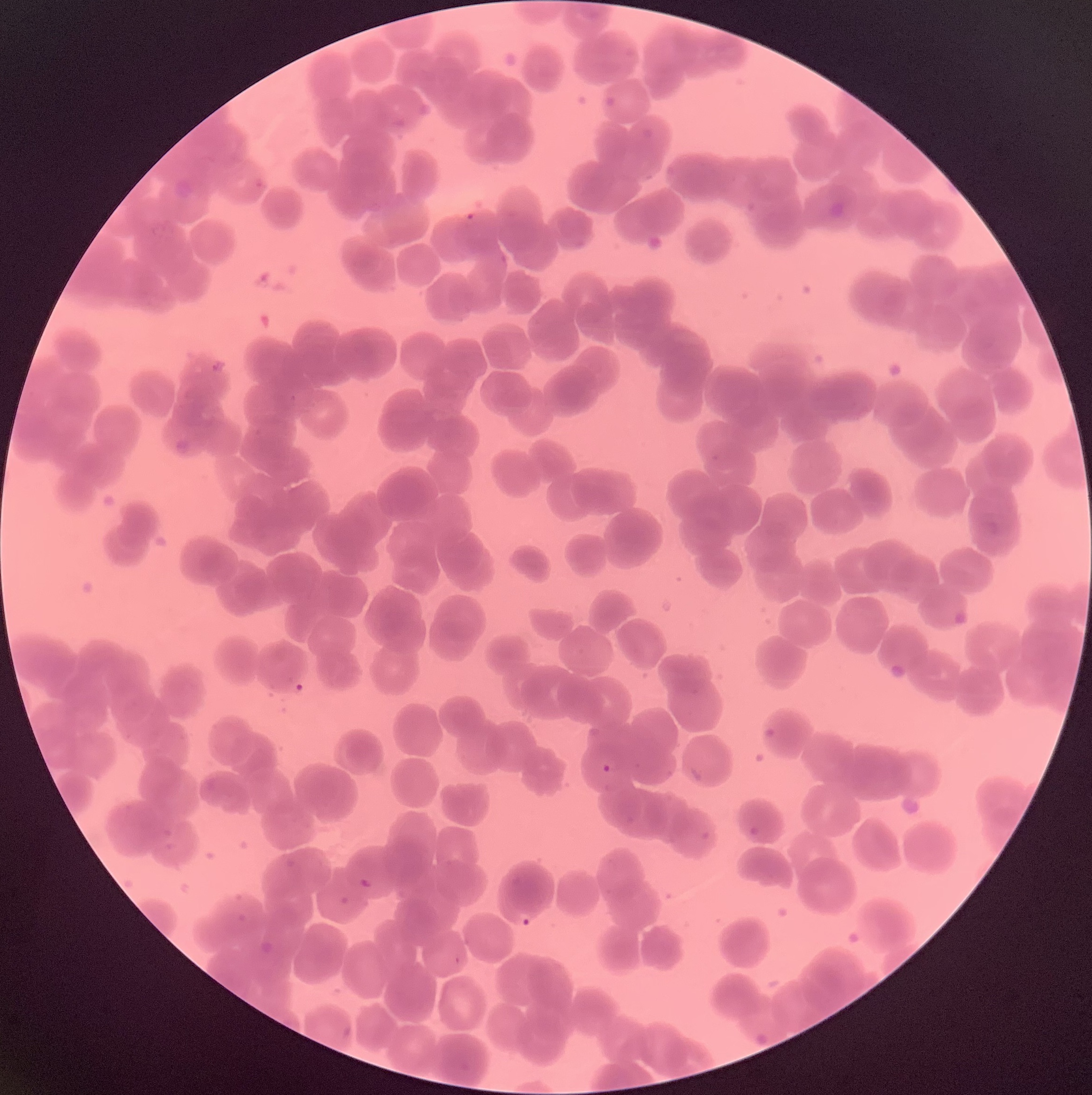
Summary:
  - Coordinate format: approximate bounding boxes as named x1/y1/x2/y2 corners in pixels
  - Plasmodium parasite locations: (x1=464, y1=212, x2=476, y2=224), (x1=600, y1=762, x2=613, y2=775), (x1=356, y1=876, x2=374, y2=890), (x1=516, y1=911, x2=535, y2=928)
  - Image size: 1092×1095 pixels
  - Red blood cell morphology: rouleaux formation
  - Modality: optical microscopy
  - Preparation: thin blood smear